Assess this cell for malaria.
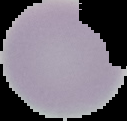

It is uninfected.

Summary:
  - Image size: 127×121 pixels
  - Preparation: thin blood film
  - Image type: segmented cell region with the area outside set to black